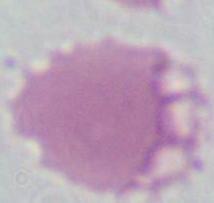
Summary:
  - Magnification: 1000x
  - Identification: red blood cell
  - Modality: micrograph